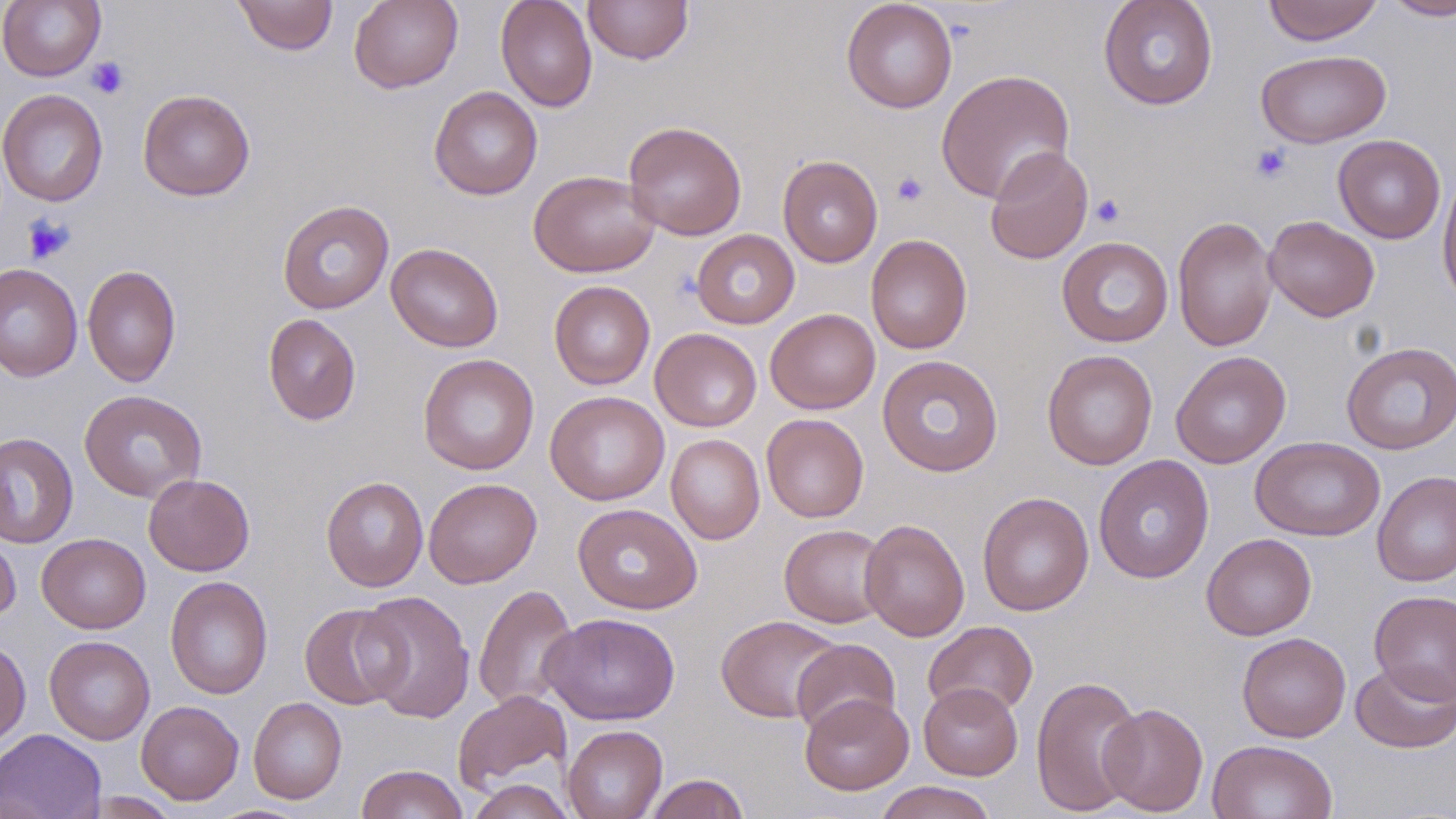

slide_level_diagnosis: no evidence of blood parasites
modality: optical microscopy
preparation: thin blood smear
magnification: 1000x
stain: May-Grünwald-Giemsa
field_of_view: single
image_size: 1456×819 pixels
uninfected_red_blood_cell_locations: 'approximate bounding boxes as named x1/y1/x2/y2 corners in pixels: (x1=232, y1=0, x2=339, y2=55), (x1=348, y1=0, x2=463, y2=93), (x1=496, y1=0, x2=597, y2=112), (x1=583, y1=0, x2=694, y2=65), (x1=841, y1=0, x2=958, y2=113), (x1=1098, y1=0, x2=1219, y2=110), (x1=1262, y1=0, x2=1383, y2=45), (x1=1382, y1=0, x2=1456, y2=21), (x1=0, y1=1, x2=105, y2=81), (x1=1256, y1=49, x2=1391, y2=148), (x1=935, y1=69, x2=1075, y2=204), (x1=429, y1=86, x2=543, y2=200), (x1=1, y1=88, x2=108, y2=207), (x1=137, y1=89, x2=255, y2=201), (x1=623, y1=121, x2=746, y2=240), (x1=1333, y1=134, x2=1446, y2=244), (x1=984, y1=145, x2=1094, y2=265), (x1=777, y1=155, x2=883, y2=267), (x1=1438, y1=168, x2=1456, y2=311), (x1=529, y1=170, x2=659, y2=277), (x1=278, y1=199, x2=394, y2=314), (x1=1172, y1=215, x2=1279, y2=353), (x1=1263, y1=215, x2=1379, y2=322), (x1=690, y1=229, x2=800, y2=329), (x1=865, y1=234, x2=972, y2=354), (x1=1056, y1=236, x2=1174, y2=348), (x1=386, y1=242, x2=503, y2=352), (x1=0, y1=263, x2=83, y2=383), (x1=82, y1=264, x2=182, y2=387), (x1=549, y1=280, x2=655, y2=389), (x1=765, y1=308, x2=880, y2=415), (x1=263, y1=313, x2=361, y2=425), (x1=650, y1=328, x2=762, y2=432), (x1=1341, y1=341, x2=1456, y2=455), (x1=1042, y1=349, x2=1158, y2=470), (x1=1171, y1=351, x2=1291, y2=469), (x1=418, y1=354, x2=539, y2=475), (x1=877, y1=355, x2=1004, y2=477), (x1=79, y1=389, x2=207, y2=503), (x1=545, y1=391, x2=669, y2=505), (x1=762, y1=414, x2=869, y2=523), (x1=0, y1=431, x2=79, y2=548), (x1=665, y1=433, x2=765, y2=545), (x1=1250, y1=436, x2=1385, y2=541), (x1=1093, y1=455, x2=1214, y2=584), (x1=1371, y1=469, x2=1456, y2=587), (x1=143, y1=473, x2=254, y2=576), (x1=321, y1=476, x2=428, y2=592), (x1=424, y1=477, x2=542, y2=589), (x1=976, y1=492, x2=1094, y2=617), (x1=572, y1=503, x2=702, y2=615), (x1=860, y1=518, x2=970, y2=641), (x1=779, y1=524, x2=890, y2=628), (x1=0, y1=530, x2=21, y2=624), (x1=37, y1=533, x2=151, y2=633), (x1=1201, y1=533, x2=1317, y2=640), (x1=165, y1=576, x2=273, y2=699), (x1=473, y1=583, x2=579, y2=713), (x1=1368, y1=589, x2=1456, y2=705), (x1=356, y1=590, x2=474, y2=723), (x1=299, y1=603, x2=407, y2=710), (x1=541, y1=612, x2=680, y2=724), (x1=715, y1=615, x2=843, y2=724), (x1=923, y1=621, x2=1038, y2=719), (x1=1236, y1=632, x2=1351, y2=742), (x1=44, y1=635, x2=155, y2=745), (x1=0, y1=639, x2=31, y2=747), (x1=791, y1=639, x2=901, y2=738), (x1=1350, y1=658, x2=1456, y2=754), (x1=1030, y1=674, x2=1145, y2=816), (x1=918, y1=682, x2=1023, y2=780), (x1=452, y1=690, x2=572, y2=792), (x1=799, y1=693, x2=914, y2=794), (x1=248, y1=696, x2=347, y2=804), (x1=136, y1=700, x2=244, y2=805), (x1=1099, y1=703, x2=1209, y2=816), (x1=562, y1=725, x2=667, y2=819), (x1=0, y1=728, x2=106, y2=819), (x1=1206, y1=739, x2=1338, y2=819), (x1=355, y1=764, x2=469, y2=819), (x1=644, y1=773, x2=749, y2=819), (x1=466, y1=778, x2=577, y2=818), (x1=872, y1=781, x2=998, y2=819), (x1=78, y1=791, x2=183, y2=818)'
platelet_locations: 'approximate bounding boxes as named x1/y1/x2/y2 corners in pixels: (x1=86, y1=57, x2=130, y2=100), (x1=1250, y1=144, x2=1292, y2=183), (x1=891, y1=171, x2=928, y2=206), (x1=1090, y1=193, x2=1125, y2=228), (x1=23, y1=214, x2=75, y2=264)'